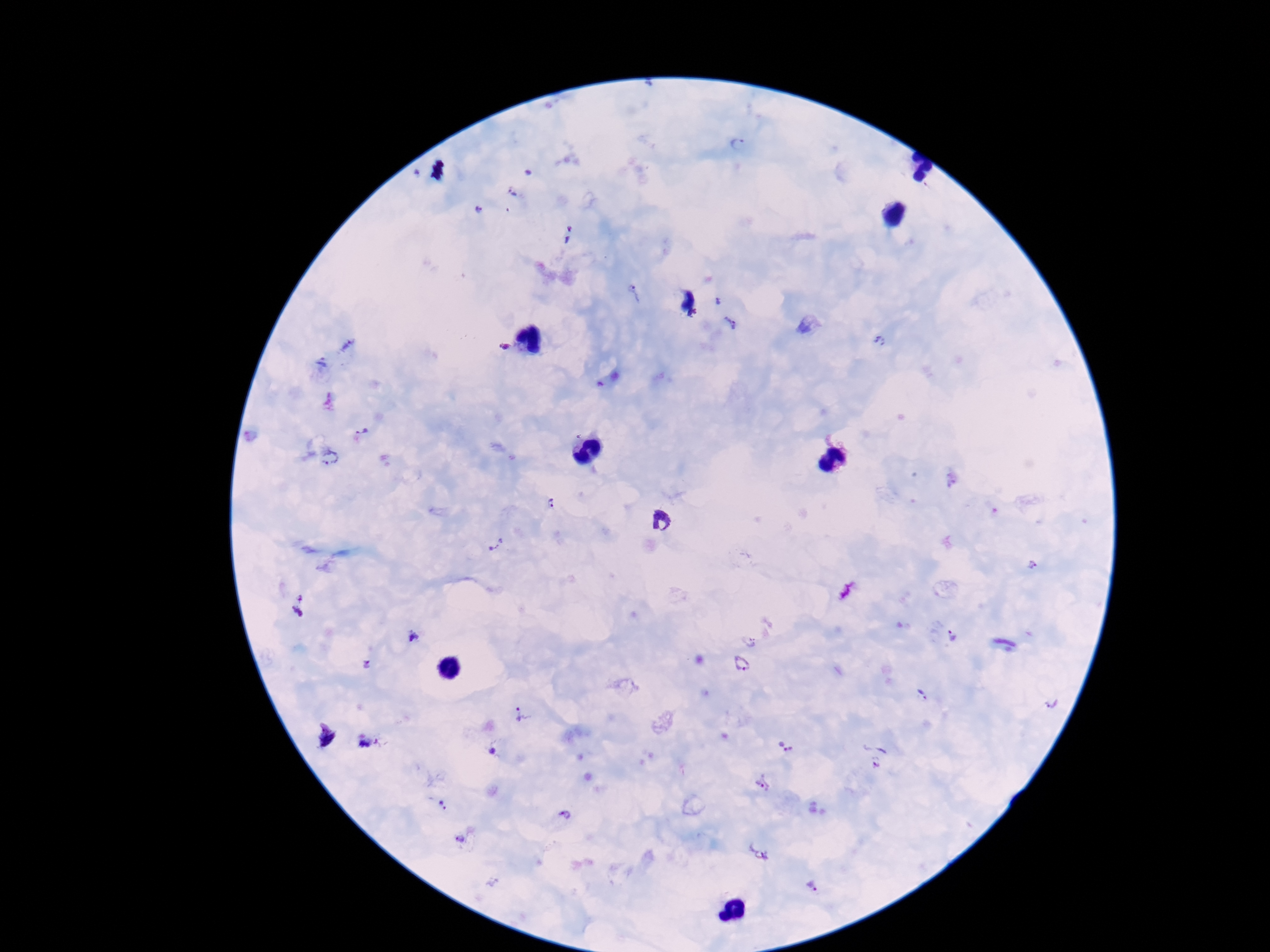 Approximate centers as [x, y] in pixels. Plasmodium parasite locations: [738, 144], [512, 195], [478, 210], [568, 235], [637, 292], [719, 300], [693, 314], [730, 322], [879, 342], [347, 344], [504, 347], [321, 363], [362, 432], [329, 459], [552, 504], [662, 522], [497, 544], [1034, 564], [299, 605], [751, 636], [415, 637], [951, 637], [369, 665], [741, 665], [922, 695], [1053, 702], [523, 715], [784, 745], [494, 752], [873, 756], [763, 784], [443, 806], [565, 815], [460, 839], [758, 853], [813, 886]. Smartphone photograph taken through the microscope eyepiece. Patient malaria status: positive. Giemsa-stained preparation. Thick peripheral-blood smear. 100x magnification. Image is 1270×952 pixels. One field from this slide.